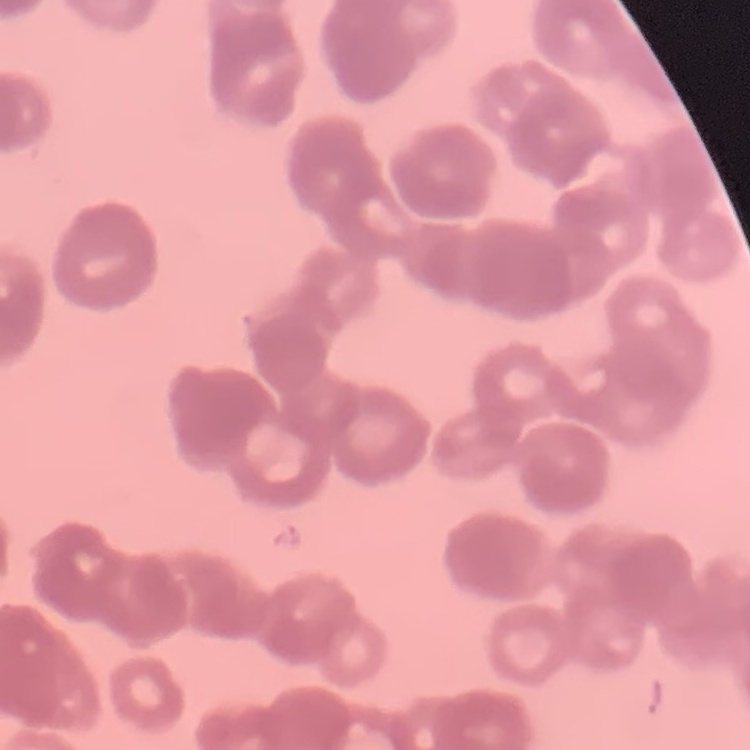
Summary:
  - Red blood cell morphology: rouleaux formation
  - Image type: square crop of a larger photomicrograph
  - Preparation: thin blood film
  - Stain: Field's or Giemsa